Classify this cell by malaria status.
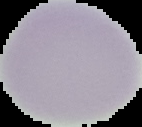

It is uninfected.

Image is 142×127 pixels. From a thin blood film. Segmented cell region on a black background.